Mark where platelets are.
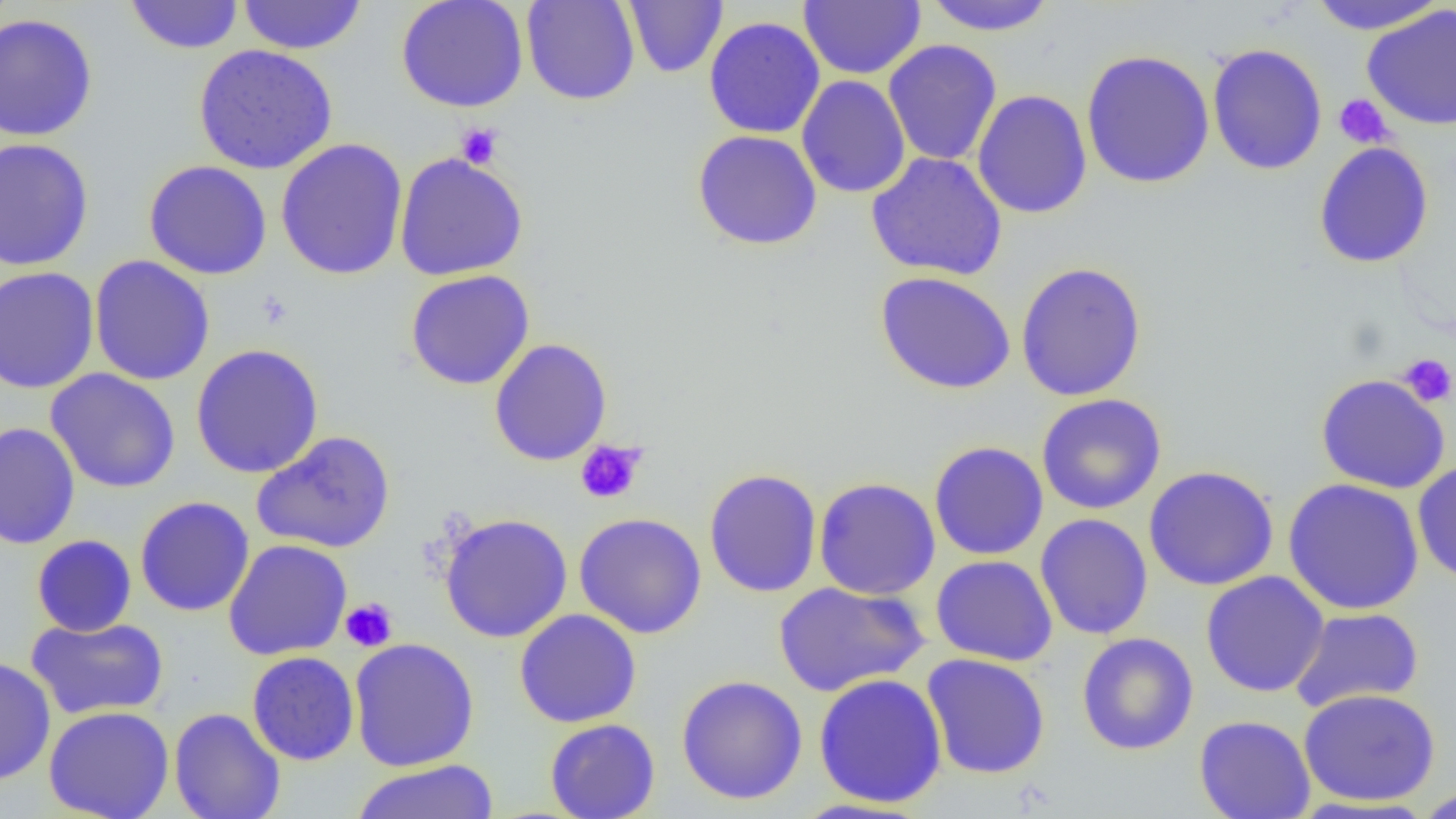
Approximate bounding boxes as (x1,y1)-(x2,y2) corner pairs in pixels.
Platelets (subset): (1334,94)-(1393,148), (456,123)-(504,169), (1398,354)-(1456,407), (575,440)-(647,505), (340,598)-(398,652).

Uninfected red blood cell locations (subset): (125,0)-(243,54), (237,0)-(367,55), (395,0)-(529,113), (521,0)-(640,105), (624,0)-(728,78), (799,0)-(925,80), (1306,0)-(1446,34), (921,1)-(1059,36), (1362,4)-(1456,132), (0,12)-(99,142), (703,16)-(825,139), (883,39)-(1002,167), (1207,43)-(1327,175), (193,44)-(338,174), (1080,49)-(1215,189), (797,75)-(910,198), (972,89)-(1092,219), (692,129)-(822,250), (0,137)-(95,272), (275,138)-(408,280), (1313,141)-(1434,269), (394,152)-(529,281), (866,152)-(1007,281), (143,159)-(273,280), (89,254)-(215,386), (1015,261)-(1147,401), (0,266)-(100,393), (404,269)-(536,390), (875,271)-(1016,395), (190,343)-(324,479), (45,368)-(181,493), (1315,373)-(1450,494), (1035,394)-(1167,515), (0,422)-(80,550), (250,431)-(396,554), (929,440)-(1048,560), (1412,460)-(1456,585), (1142,466)-(1279,591), (704,468)-(822,598), (813,477)-(941,599), (1282,478)-(1424,615), (134,496)-(255,617), (574,511)-(707,639), (439,513)-(573,643), (1035,513)-(1154,640), (31,534)-(137,637), (223,539)-(352,661), (931,555)-(1058,666), (1200,571)-(1329,697), (773,581)-(930,697), (1289,607)-(1424,712), (514,609)-(642,728), (25,616)-(169,720), (1076,632)-(1199,755), (349,638)-(480,771), (247,651)-(360,766), (921,653)-(1051,779), (0,655)-(56,786), (813,673)-(947,808), (676,674)-(808,805), (1298,688)-(1441,807), (44,705)-(174,819), (168,707)-(285,819), (1194,714)-(1316,819), (544,718)-(660,819), (350,760)-(499,819), (1413,786)-(1456,818), (787,797)-(931,818). Slide-level diagnosis: no evidence of blood parasites. Thin blood film. Image is 1456×819 pixels. 1000x magnification. Optical microscopy. One field of a larger specimen.